Locate every Plasmodium falciparum-infected red blood cell.
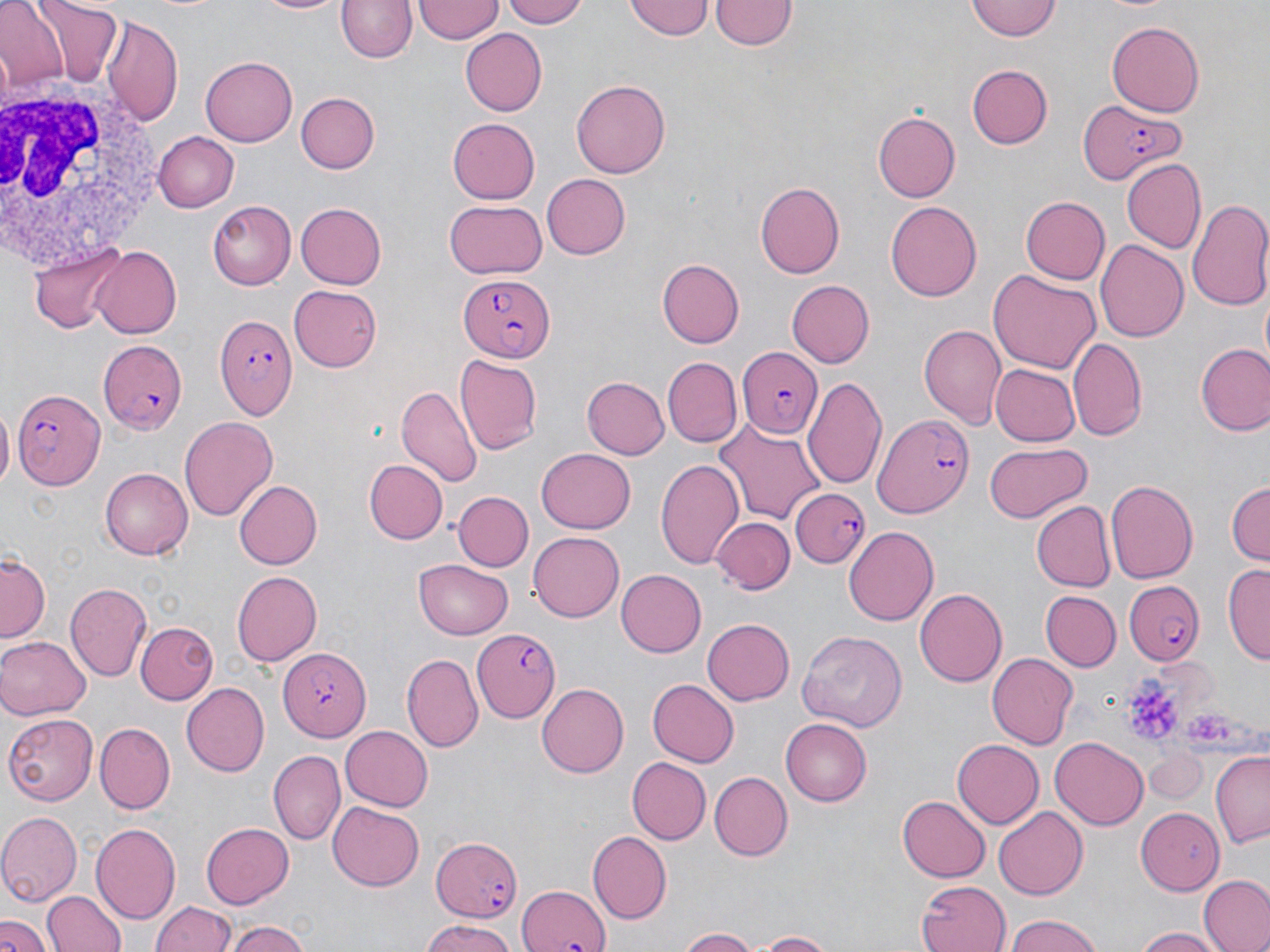

Approximate bounding boxes as named x1/y1/x2/y2 corners in pixels.
Plasmodium falciparum-infected red blood cells: (x1=1078, y1=106, x2=1185, y2=181), (x1=458, y1=272, x2=553, y2=362), (x1=216, y1=314, x2=298, y2=422), (x1=99, y1=339, x2=186, y2=435), (x1=736, y1=347, x2=823, y2=437), (x1=11, y1=389, x2=103, y2=491), (x1=872, y1=413, x2=977, y2=519), (x1=789, y1=488, x2=868, y2=569), (x1=1121, y1=584, x2=1207, y2=662), (x1=475, y1=626, x2=560, y2=722), (x1=277, y1=648, x2=371, y2=741), (x1=431, y1=835, x2=525, y2=921), (x1=515, y1=876, x2=615, y2=952).

Summary:
  - White blood cell locations: (x1=1, y1=87, x2=169, y2=274)
  - Uninfected red blood cell locations: (x1=32, y1=0, x2=124, y2=87), (x1=254, y1=0, x2=345, y2=15), (x1=335, y1=0, x2=417, y2=64), (x1=503, y1=0, x2=592, y2=28), (x1=623, y1=0, x2=714, y2=41), (x1=710, y1=0, x2=797, y2=51), (x1=966, y1=0, x2=1059, y2=41), (x1=0, y1=1, x2=68, y2=89), (x1=415, y1=1, x2=503, y2=45), (x1=104, y1=16, x2=183, y2=126), (x1=1106, y1=19, x2=1205, y2=116), (x1=459, y1=28, x2=547, y2=116), (x1=201, y1=57, x2=297, y2=147), (x1=966, y1=63, x2=1053, y2=149), (x1=571, y1=80, x2=671, y2=178), (x1=296, y1=92, x2=380, y2=173), (x1=872, y1=108, x2=961, y2=204), (x1=448, y1=119, x2=541, y2=204), (x1=152, y1=131, x2=239, y2=212), (x1=1122, y1=158, x2=1207, y2=252), (x1=539, y1=173, x2=629, y2=261), (x1=756, y1=181, x2=845, y2=278), (x1=1020, y1=196, x2=1110, y2=284), (x1=1186, y1=197, x2=1270, y2=311), (x1=206, y1=198, x2=294, y2=290), (x1=444, y1=201, x2=548, y2=278), (x1=885, y1=201, x2=983, y2=301), (x1=293, y1=202, x2=386, y2=290), (x1=1095, y1=237, x2=1190, y2=341), (x1=30, y1=242, x2=127, y2=333), (x1=90, y1=245, x2=181, y2=338), (x1=658, y1=259, x2=744, y2=347), (x1=988, y1=267, x2=1102, y2=373), (x1=787, y1=280, x2=875, y2=366), (x1=288, y1=285, x2=382, y2=372), (x1=918, y1=324, x2=1006, y2=429), (x1=1068, y1=337, x2=1148, y2=443), (x1=1195, y1=342, x2=1270, y2=435), (x1=455, y1=356, x2=541, y2=456), (x1=664, y1=358, x2=741, y2=447), (x1=991, y1=364, x2=1079, y2=447), (x1=803, y1=375, x2=889, y2=489), (x1=582, y1=376, x2=669, y2=459), (x1=396, y1=386, x2=481, y2=489), (x1=0, y1=406, x2=13, y2=492), (x1=179, y1=416, x2=278, y2=522), (x1=714, y1=420, x2=825, y2=527), (x1=985, y1=443, x2=1088, y2=522), (x1=537, y1=449, x2=635, y2=532), (x1=654, y1=457, x2=745, y2=568), (x1=363, y1=459, x2=447, y2=544), (x1=101, y1=468, x2=193, y2=559), (x1=233, y1=479, x2=322, y2=569), (x1=1105, y1=479, x2=1198, y2=586), (x1=1226, y1=480, x2=1269, y2=565), (x1=455, y1=491, x2=532, y2=571), (x1=1030, y1=501, x2=1116, y2=591), (x1=712, y1=508, x2=799, y2=669), (x1=713, y1=516, x2=794, y2=593), (x1=843, y1=526, x2=939, y2=625), (x1=529, y1=532, x2=625, y2=622), (x1=0, y1=553, x2=51, y2=641), (x1=414, y1=560, x2=514, y2=640), (x1=1225, y1=563, x2=1270, y2=665), (x1=231, y1=568, x2=321, y2=663), (x1=614, y1=569, x2=707, y2=658), (x1=66, y1=583, x2=153, y2=682), (x1=915, y1=587, x2=1007, y2=686), (x1=1041, y1=591, x2=1121, y2=670), (x1=702, y1=618, x2=796, y2=704), (x1=139, y1=623, x2=217, y2=705), (x1=796, y1=628, x2=907, y2=732), (x1=0, y1=637, x2=87, y2=721), (x1=402, y1=652, x2=483, y2=751), (x1=987, y1=654, x2=1078, y2=749), (x1=646, y1=678, x2=739, y2=766), (x1=181, y1=683, x2=269, y2=775), (x1=535, y1=684, x2=626, y2=777), (x1=4, y1=713, x2=99, y2=803), (x1=781, y1=719, x2=873, y2=807), (x1=95, y1=723, x2=175, y2=811), (x1=339, y1=725, x2=433, y2=811), (x1=1051, y1=735, x2=1149, y2=829), (x1=953, y1=739, x2=1043, y2=828), (x1=1144, y1=747, x2=1209, y2=806), (x1=269, y1=750, x2=345, y2=843), (x1=1210, y1=752, x2=1269, y2=849), (x1=629, y1=757, x2=711, y2=843), (x1=710, y1=772, x2=792, y2=862), (x1=898, y1=795, x2=990, y2=879), (x1=328, y1=802, x2=424, y2=891), (x1=993, y1=806, x2=1086, y2=899), (x1=1135, y1=807, x2=1222, y2=894), (x1=0, y1=811, x2=80, y2=904), (x1=200, y1=821, x2=294, y2=909), (x1=89, y1=822, x2=181, y2=923), (x1=588, y1=831, x2=671, y2=922), (x1=1199, y1=875, x2=1270, y2=952), (x1=919, y1=879, x2=1012, y2=952), (x1=42, y1=889, x2=126, y2=952), (x1=151, y1=898, x2=236, y2=952), (x1=1003, y1=915, x2=1107, y2=952), (x1=1, y1=917, x2=50, y2=952), (x1=228, y1=919, x2=311, y2=952), (x1=417, y1=924, x2=520, y2=952), (x1=1132, y1=924, x2=1223, y2=952), (x1=675, y1=927, x2=761, y2=952), (x1=747, y1=931, x2=837, y2=951)
  - Platelet locations: (x1=1122, y1=660, x2=1204, y2=748)
  - Slide-level diagnosis: Plasmodium falciparum
  - Magnification: 1000x
  - Image size: 1270×952 pixels
  - Modality: optical microscopy
  - Stain: May-Grünwald-Giemsa
  - Preparation: thin blood film
  - Field of view: single